Classify this cell by malaria status.
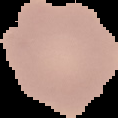
Uninfected.

Summary:
  - Image size: 118×118 pixels
  - Image type: segmented cell region with the area outside set to black
  - Preparation: thin blood smear